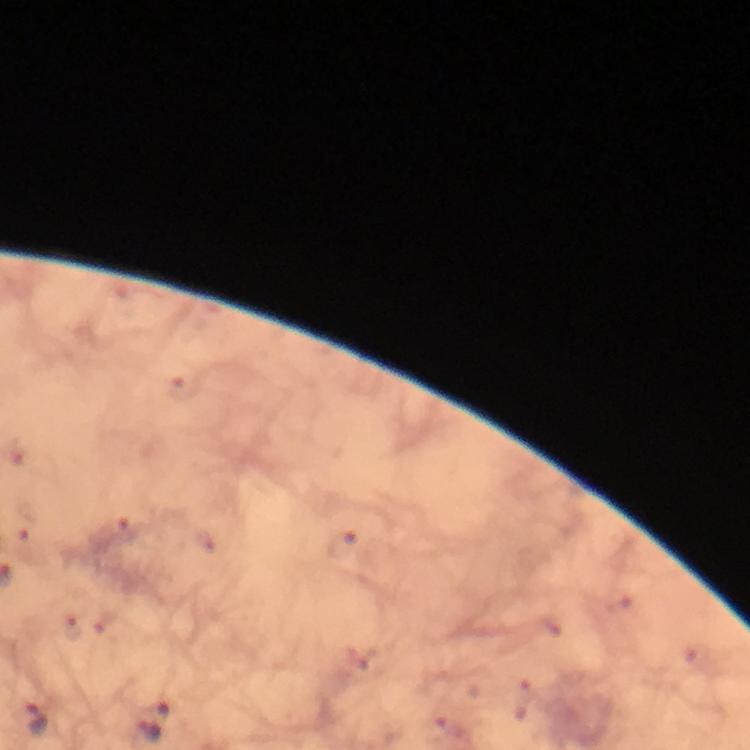
capture = smartphone mounted on the microscope
immersion oil = used
stain = Giemsa
context = from a malaria diagnostic workup
Plasmodium parasite locations = approximate centers as (x, y) in pixels: (38, 719), (156, 719)
preparation = thick blood smear
cropped from = one field of view
magnification = 100x
image size = 750×750 pixels